Comment on the morphology of the red blood cells.
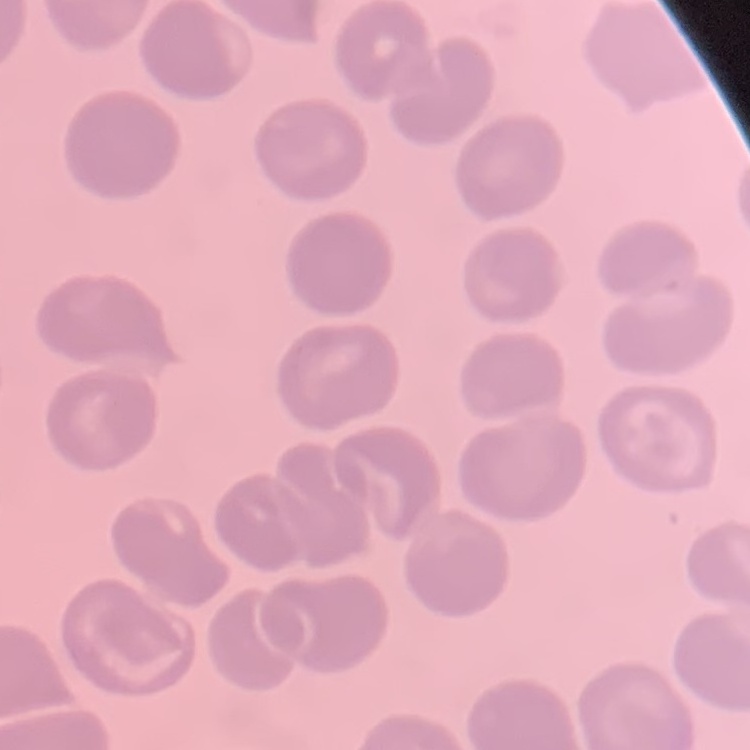
They show no rouleaux formation.

Stained with either Field's or Giemsa. Thin blood smear. One tile cut from a larger photomicrograph.